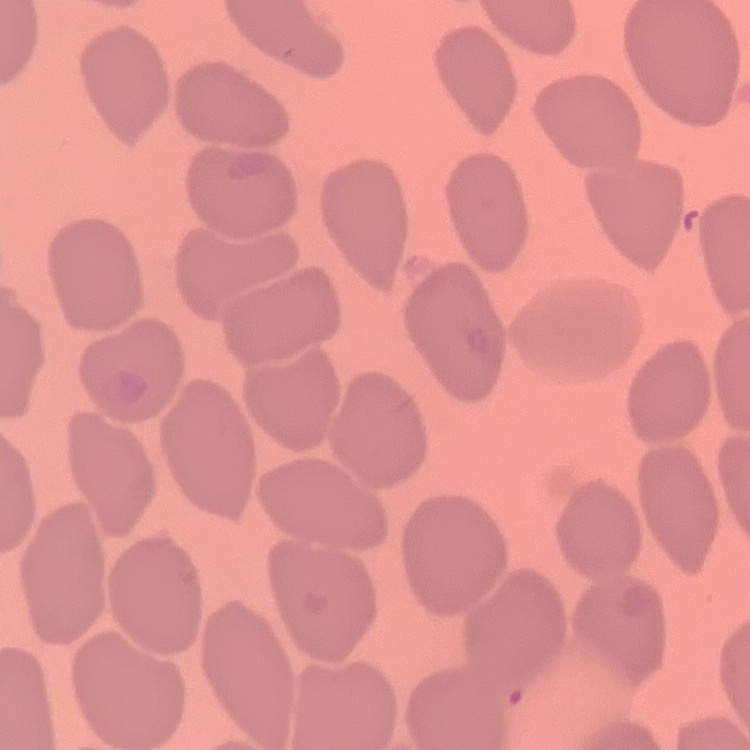 The erythrocytes show no rouleaux formation. Thin blood smear. Field's or Giemsa stain. Square crop of a larger photomicrograph.